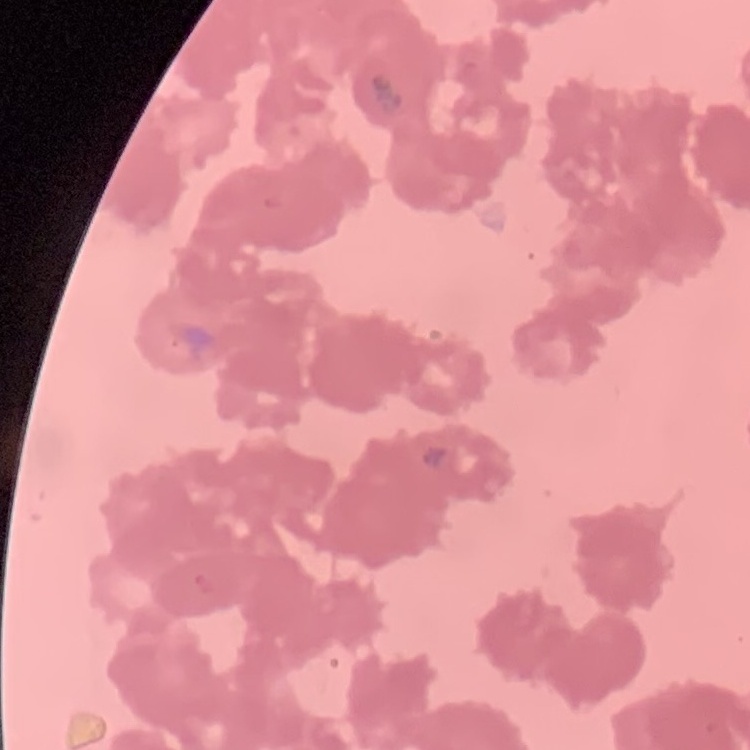

The erythrocytes exhibit rouleaux formation. Thin peripheral smear. Field's or Giemsa stain. One tile cut from a larger photomicrograph.